Report the malaria status of this cell.
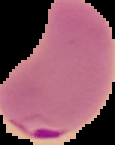
It is parasitized.

image size = 115×145 pixels
preparation = thin blood film
image type = cell region segmented out of the field of view; surrounding area masked to black